State which parasite is depicted.
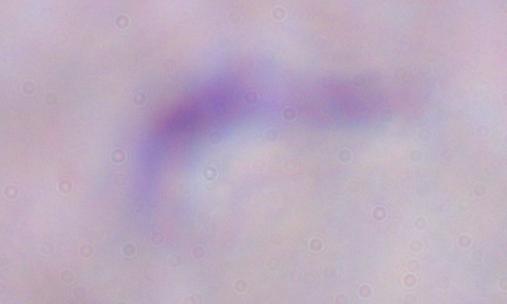
This is a trypanosome.

Captured at 1000x magnification. Micrograph.